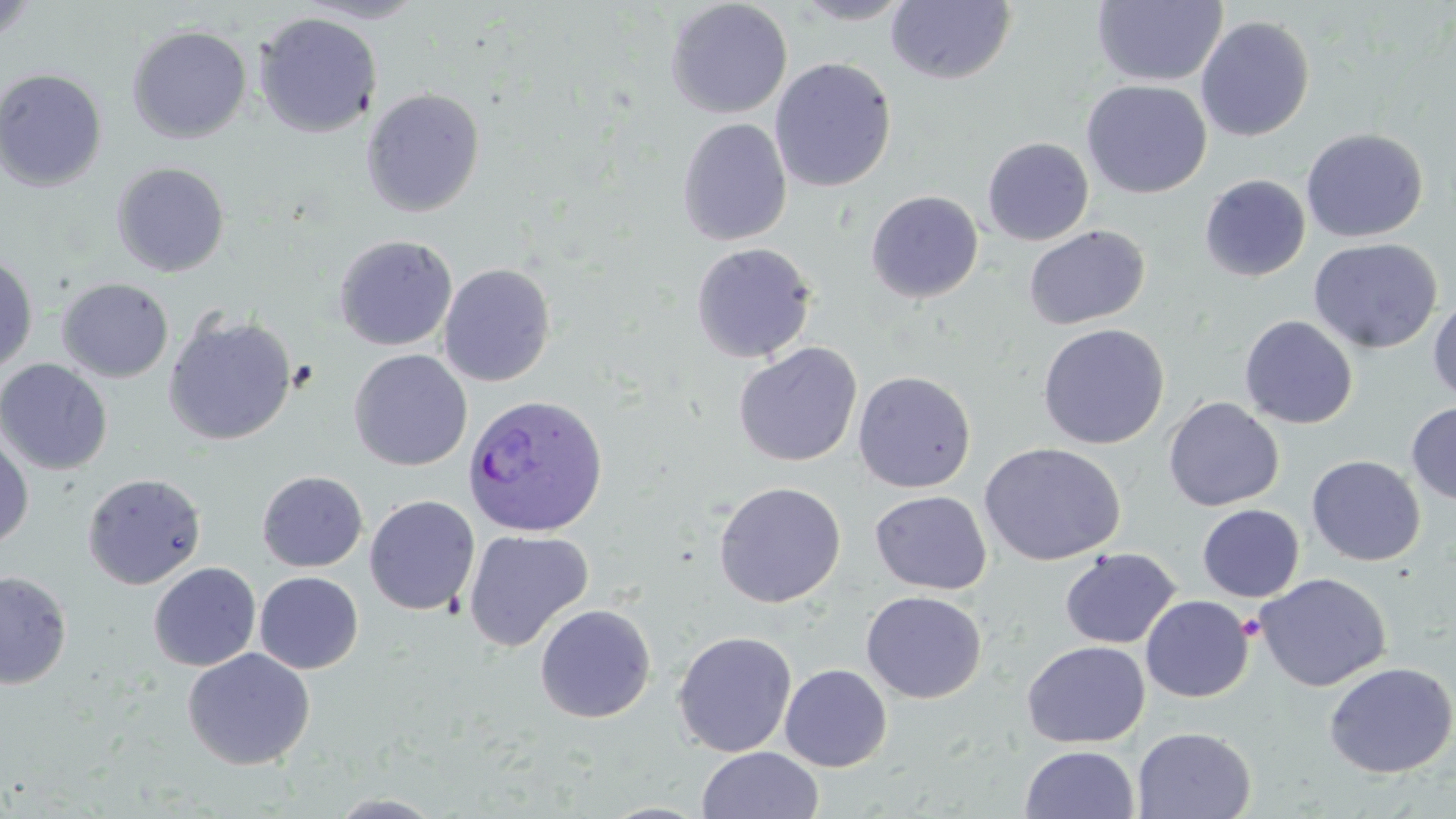
Approximate bounding boxes as named x1/y1/x2/y2 corners in pixels. Plasmodium ovale-infected red blood cell locations: (x1=462, y1=393, x2=609, y2=537). Platelet locations: (x1=1237, y1=614, x2=1264, y2=642). Uninfected red blood cell locations: (x1=296, y1=0, x2=430, y2=24), (x1=665, y1=0, x2=793, y2=119), (x1=792, y1=0, x2=916, y2=25), (x1=886, y1=0, x2=1016, y2=85), (x1=1092, y1=0, x2=1227, y2=87), (x1=0, y1=1, x2=38, y2=46), (x1=254, y1=12, x2=382, y2=138), (x1=1195, y1=15, x2=1315, y2=142), (x1=126, y1=25, x2=252, y2=144), (x1=769, y1=57, x2=897, y2=192), (x1=0, y1=68, x2=107, y2=192), (x1=1082, y1=79, x2=1211, y2=198), (x1=361, y1=88, x2=486, y2=217), (x1=677, y1=117, x2=792, y2=246), (x1=1301, y1=128, x2=1428, y2=243), (x1=981, y1=136, x2=1094, y2=246), (x1=111, y1=162, x2=230, y2=277), (x1=1199, y1=174, x2=1310, y2=282), (x1=865, y1=190, x2=984, y2=303), (x1=1023, y1=225, x2=1150, y2=330), (x1=333, y1=234, x2=458, y2=351), (x1=1308, y1=238, x2=1442, y2=354), (x1=690, y1=242, x2=817, y2=364), (x1=0, y1=253, x2=38, y2=375), (x1=438, y1=263, x2=557, y2=387), (x1=57, y1=277, x2=174, y2=383), (x1=1428, y1=298, x2=1456, y2=403), (x1=163, y1=312, x2=297, y2=446), (x1=1239, y1=315, x2=1358, y2=429), (x1=1037, y1=323, x2=1169, y2=450), (x1=733, y1=342, x2=863, y2=467), (x1=349, y1=349, x2=472, y2=471), (x1=0, y1=358, x2=113, y2=475), (x1=853, y1=371, x2=976, y2=493), (x1=1163, y1=397, x2=1284, y2=511), (x1=1406, y1=401, x2=1456, y2=506), (x1=0, y1=434, x2=33, y2=549), (x1=979, y1=442, x2=1126, y2=566), (x1=1306, y1=455, x2=1426, y2=566), (x1=257, y1=471, x2=368, y2=573), (x1=82, y1=472, x2=207, y2=590), (x1=713, y1=481, x2=846, y2=608), (x1=870, y1=490, x2=992, y2=595), (x1=364, y1=495, x2=480, y2=616), (x1=1197, y1=504, x2=1304, y2=602), (x1=463, y1=529, x2=594, y2=652), (x1=1060, y1=548, x2=1181, y2=649), (x1=148, y1=562, x2=261, y2=672), (x1=0, y1=570, x2=72, y2=691), (x1=254, y1=571, x2=363, y2=674), (x1=1256, y1=572, x2=1392, y2=691), (x1=861, y1=591, x2=986, y2=703), (x1=1140, y1=595, x2=1254, y2=703), (x1=535, y1=604, x2=656, y2=723), (x1=672, y1=631, x2=797, y2=758), (x1=1021, y1=640, x2=1150, y2=748), (x1=182, y1=647, x2=316, y2=771), (x1=1323, y1=661, x2=1456, y2=778), (x1=780, y1=663, x2=892, y2=771), (x1=1133, y1=726, x2=1256, y2=818), (x1=1019, y1=745, x2=1140, y2=819), (x1=696, y1=747, x2=825, y2=819), (x1=326, y1=793, x2=449, y2=818). Slide-level diagnosis: Plasmodium ovale. One field of a larger specimen. May-Grünwald-Giemsa stain. Image is 1456×819 pixels. 1000x magnification. Light microscopy. Thin blood smear.